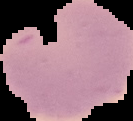 Cell region segmented out of the field of view; the surrounding area is masked to black. From a thin blood film. Malaria status: uninfected. Image is 133×121 pixels.